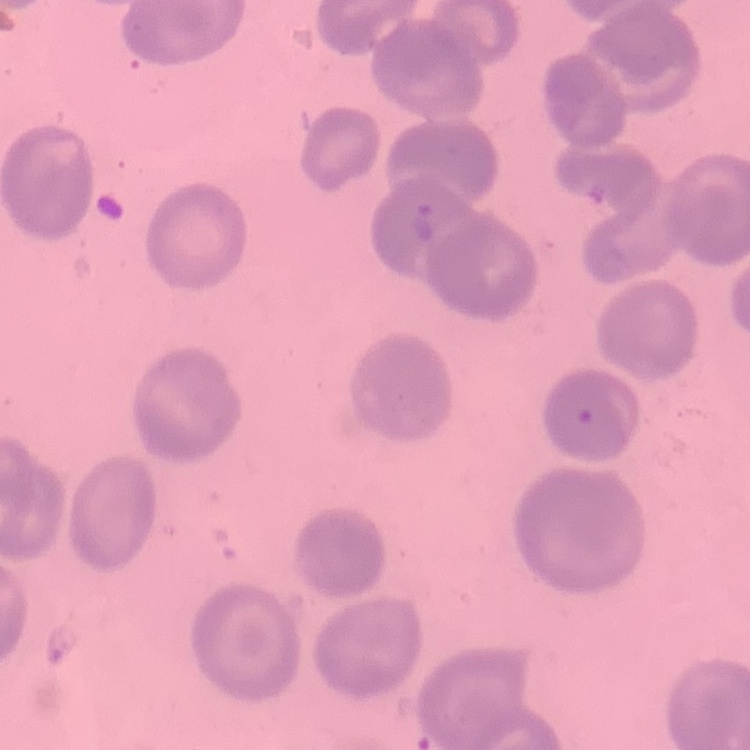
Summary:
  - Erythrocyte morphology: no rouleaux formation
  - Preparation: thin blood film
  - Image type: one tile cut from a larger photomicrograph
  - Stain: Field's or Giemsa